Outline each Plasmodium falciparum parasite and classify it by life-cycle stage.
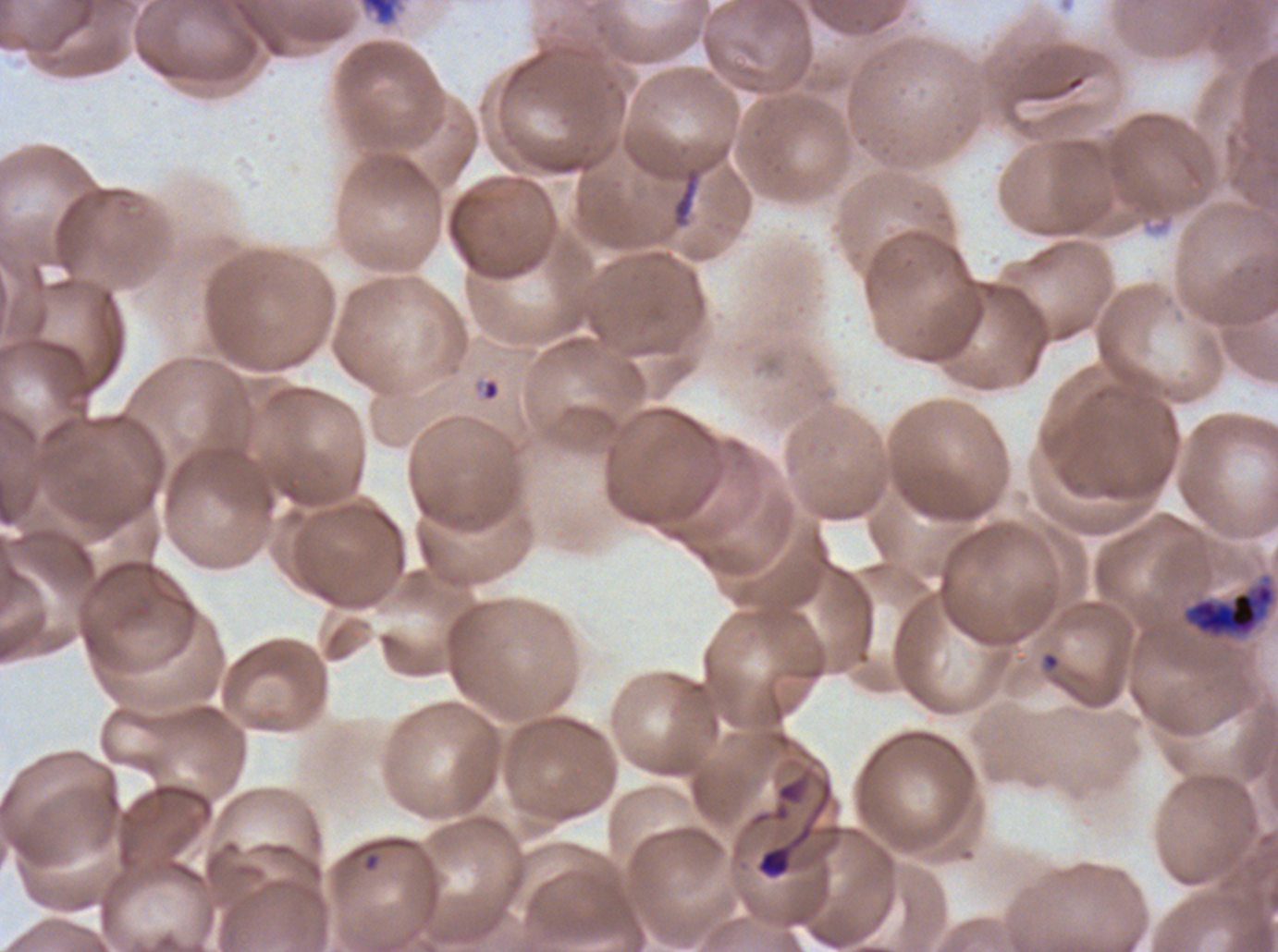

Approximate bounding boxes as [x1, y1, x2, y2] in pixels.
Rings: [483, 380, 499, 400], [1043, 653, 1059, 669].
Early schizonts: [359, 0, 401, 26], [1181, 574, 1277, 640].
No late-ring/early-trophozoite forms, mid trophozoites, late trophozoites, late schizonts, segmenters, or gametocytes observed.

{
  "stain": "Giemsa",
  "preparation": "thin blood smear",
  "image_size": "1278×952 pixels",
  "specimen": "Plasmodium falciparum from a patient in The Gambia, cultured ex vivo for 24 to 48 hours",
  "debris_locations": "approximate bounding boxes as [x1, y1, x2, y2] in pixels: [672, 170, 700, 226], [756, 845, 792, 879]",
  "field_of_view": "one sub-image of a larger composite",
  "life_cycle_stages_observed": "ring, early schizont"
}